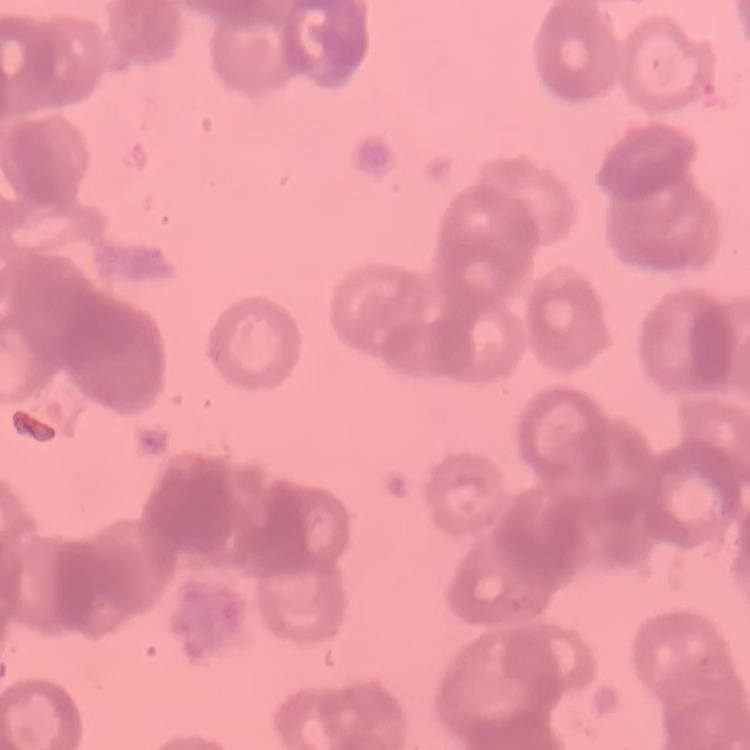

Summary:
  - Erythrocyte morphology: rouleaux formation
  - Stain: Field's or Giemsa
  - Image type: square crop of a larger photomicrograph
  - Preparation: thin peripheral smear